Report the malaria status of this cell.
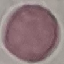

It is uninfected.

capture = smartphone through the microscope eyepiece
preparation = thin blood film
image type = automatically extracted cell patch, resized to 64 × 64 pixels
stain = Giemsa